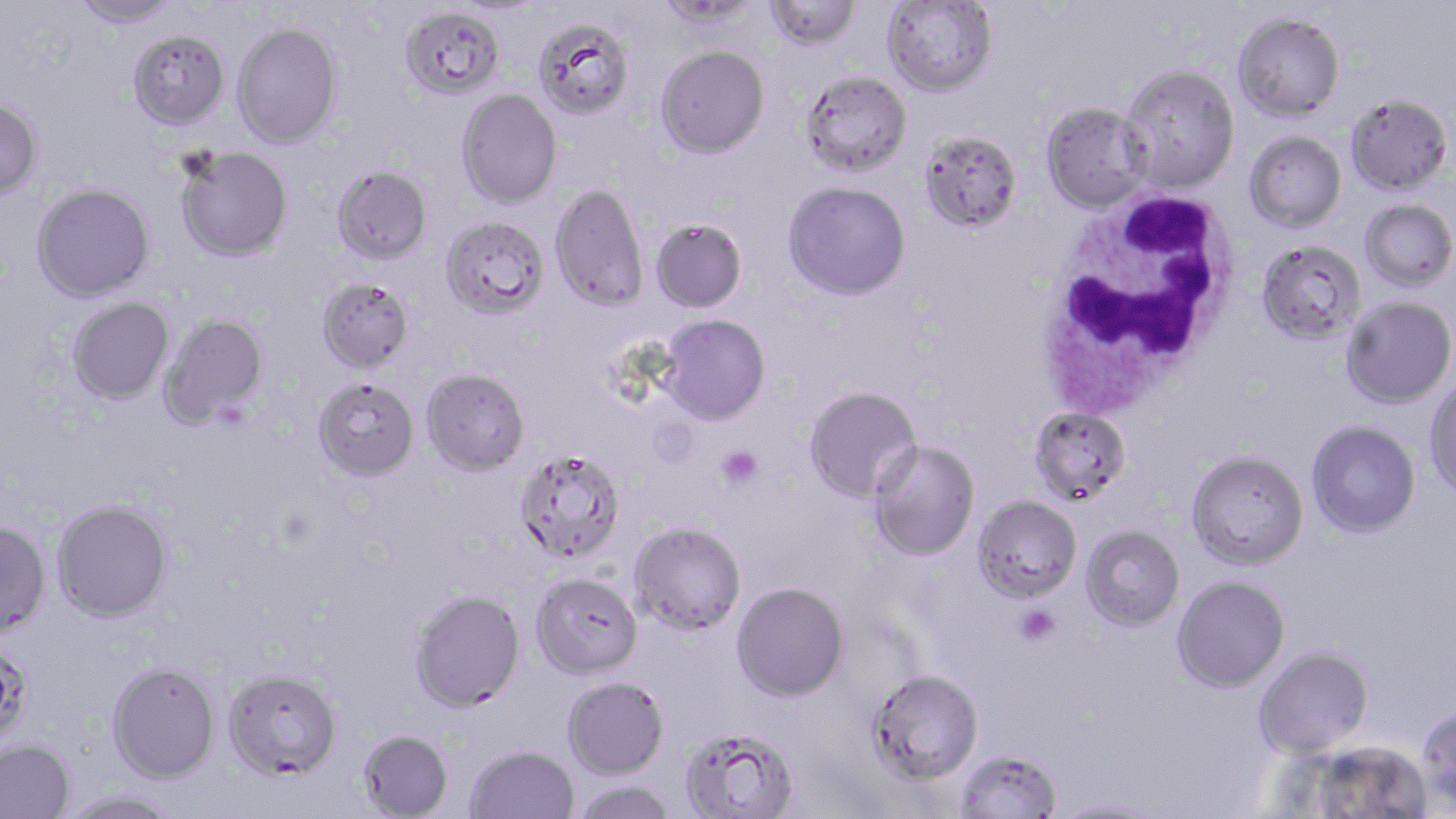
Approximate bounding boxes as (x1,y1)-(x2,y2) corner pairs in pixels. Uninfected red blood cell locations: (71,0)-(181,28), (655,0)-(760,26), (763,0)-(862,52), (882,0)-(998,96), (400,6)-(505,100), (1232,13)-(1345,122), (533,17)-(636,122), (232,22)-(342,149), (128,29)-(230,130), (655,45)-(770,158), (1120,65)-(1240,192), (801,70)-(912,177), (457,88)-(562,209), (1346,94)-(1453,196), (0,97)-(43,201), (1040,102)-(1153,213), (918,130)-(1023,233), (1244,131)-(1347,233), (175,146)-(293,263), (332,166)-(432,265), (782,180)-(911,301), (32,183)-(155,302), (550,183)-(649,313), (1359,199)-(1456,291), (441,216)-(550,321), (650,217)-(747,313), (1255,239)-(1366,346), (317,278)-(414,374), (1340,295)-(1456,408), (67,297)-(175,405), (159,314)-(269,429), (657,314)-(771,426), (421,370)-(530,477), (1424,376)-(1456,499), (312,380)-(420,483), (803,385)-(923,504), (1029,406)-(1132,505), (1306,420)-(1421,538), (867,439)-(981,562), (1186,449)-(1309,570), (513,451)-(626,565), (972,495)-(1083,603), (52,501)-(173,622), (0,521)-(51,639), (628,522)-(747,636), (1080,524)-(1185,630), (530,574)-(644,681), (1172,575)-(1291,692), (731,581)-(850,702), (409,591)-(526,715), (0,641)-(33,745), (1253,647)-(1374,758), (107,662)-(220,783), (222,669)-(341,780), (867,669)-(983,784), (562,677)-(669,779), (1416,705)-(1456,813), (680,727)-(800,819), (358,731)-(453,819), (0,740)-(75,819), (1308,740)-(1432,818), (465,745)-(580,819), (955,748)-(1063,818), (571,780)-(679,819), (58,790)-(182,818), (1048,798)-(1165,818). Platelet locations: (212,399)-(253,434), (716,445)-(763,490), (1015,605)-(1060,646). White blood cell locations: (1032,187)-(1246,415). Slide-level diagnosis: Plasmodium falciparum. May-Grünwald-Giemsa stain. Captured at 1000x magnification. Optical microscopy. Thin blood smear. Image is 1456×819 pixels. Single field of view.